Locate and identify every blood parasite.
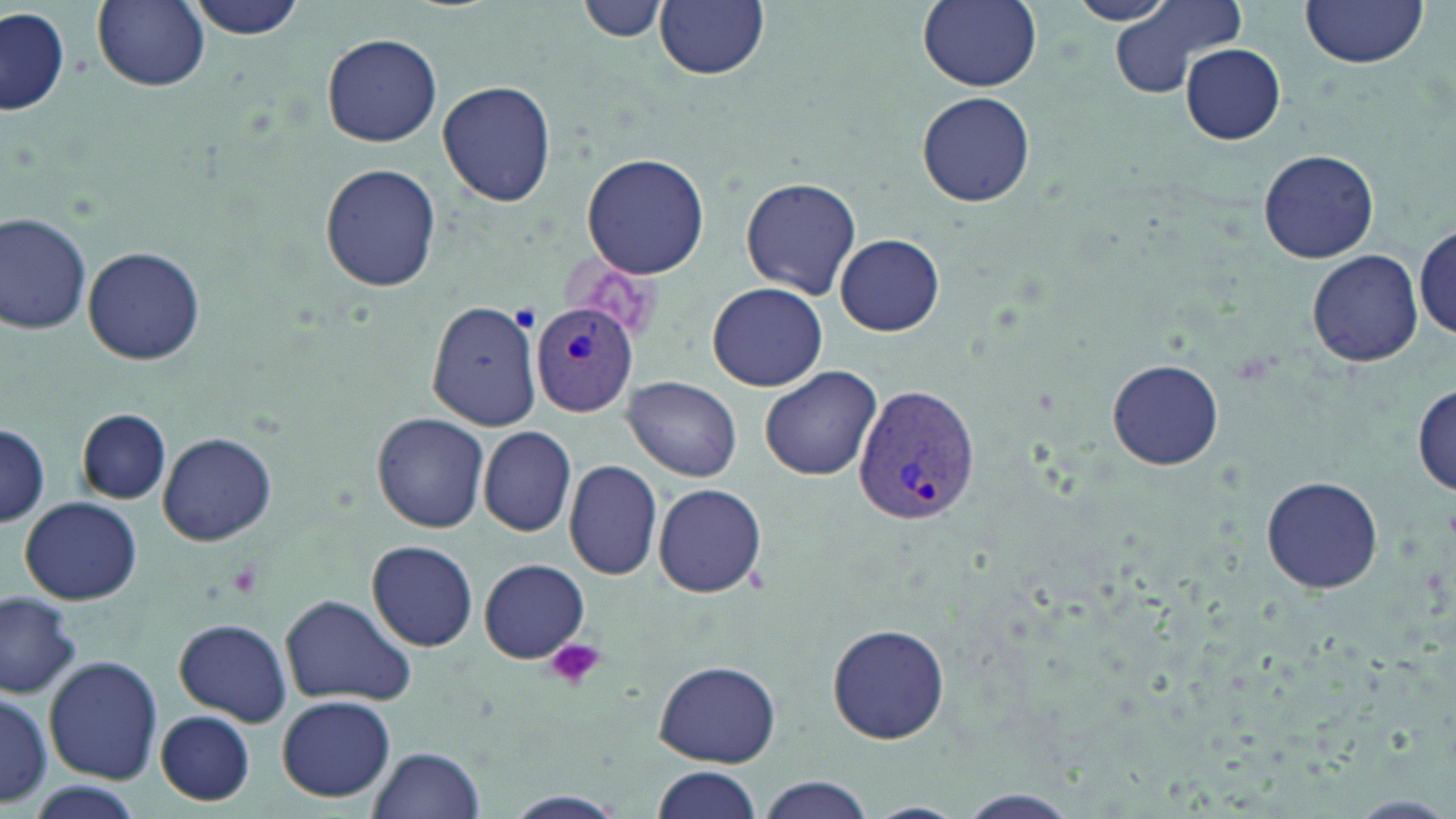

Approximate bounding boxes as named x1/y1/x2/y2 corners in pixels.
Plasmodium vivax-infected red blood cells: (x1=533, y1=302, x2=640, y2=418), (x1=854, y1=386, x2=981, y2=526).
No Plasmodium falciparum, Plasmodium ovale, Plasmodium malariae, Babesia divergens, or Trypanosoma brucei observed.

Summary:
  - Uninfected red blood cell locations: (x1=92, y1=0, x2=209, y2=92), (x1=184, y1=0, x2=308, y2=41), (x1=579, y1=0, x2=665, y2=45), (x1=656, y1=0, x2=769, y2=80), (x1=917, y1=0, x2=1043, y2=91), (x1=1067, y1=0, x2=1176, y2=25), (x1=1298, y1=0, x2=1430, y2=68), (x1=1108, y1=1, x2=1245, y2=98), (x1=1, y1=7, x2=68, y2=116), (x1=322, y1=32, x2=443, y2=147), (x1=1180, y1=42, x2=1286, y2=144), (x1=438, y1=79, x2=555, y2=208), (x1=916, y1=91, x2=1036, y2=207), (x1=1257, y1=148, x2=1379, y2=262), (x1=582, y1=153, x2=709, y2=280), (x1=320, y1=164, x2=442, y2=291), (x1=740, y1=176, x2=862, y2=300), (x1=0, y1=212, x2=96, y2=335), (x1=1414, y1=224, x2=1455, y2=341), (x1=835, y1=234, x2=944, y2=335), (x1=82, y1=246, x2=205, y2=364), (x1=1305, y1=250, x2=1424, y2=367), (x1=707, y1=282, x2=830, y2=391), (x1=427, y1=298, x2=541, y2=430), (x1=1106, y1=359, x2=1224, y2=471), (x1=760, y1=364, x2=882, y2=481), (x1=626, y1=376, x2=743, y2=482), (x1=1413, y1=383, x2=1454, y2=495), (x1=78, y1=408, x2=170, y2=503), (x1=372, y1=412, x2=487, y2=532), (x1=0, y1=423, x2=49, y2=528), (x1=479, y1=427, x2=576, y2=537), (x1=157, y1=431, x2=277, y2=546), (x1=564, y1=458, x2=663, y2=580), (x1=1260, y1=475, x2=1384, y2=594), (x1=653, y1=483, x2=767, y2=598), (x1=19, y1=497, x2=141, y2=606), (x1=368, y1=540, x2=479, y2=652), (x1=479, y1=559, x2=589, y2=663), (x1=0, y1=589, x2=80, y2=697), (x1=279, y1=594, x2=413, y2=707), (x1=172, y1=618, x2=292, y2=726), (x1=827, y1=623, x2=950, y2=744), (x1=43, y1=655, x2=163, y2=784), (x1=655, y1=658, x2=782, y2=767), (x1=0, y1=686, x2=51, y2=810), (x1=276, y1=695, x2=396, y2=803), (x1=155, y1=710, x2=256, y2=806), (x1=370, y1=745, x2=483, y2=817), (x1=648, y1=765, x2=763, y2=819), (x1=754, y1=775, x2=876, y2=819), (x1=18, y1=783, x2=148, y2=819), (x1=951, y1=789, x2=1082, y2=819), (x1=491, y1=790, x2=634, y2=819), (x1=1338, y1=795, x2=1456, y2=819), (x1=860, y1=801, x2=971, y2=819)
  - Platelet locations: (x1=544, y1=638, x2=606, y2=692)
  - Slide-level diagnosis: Plasmodium vivax
  - Modality: light microscopy
  - Preparation: thin blood film
  - Field of view: one of a larger specimen
  - Image size: 1456×819 pixels
  - Magnification: 1000x
  - Stain: May-Grünwald-Giemsa